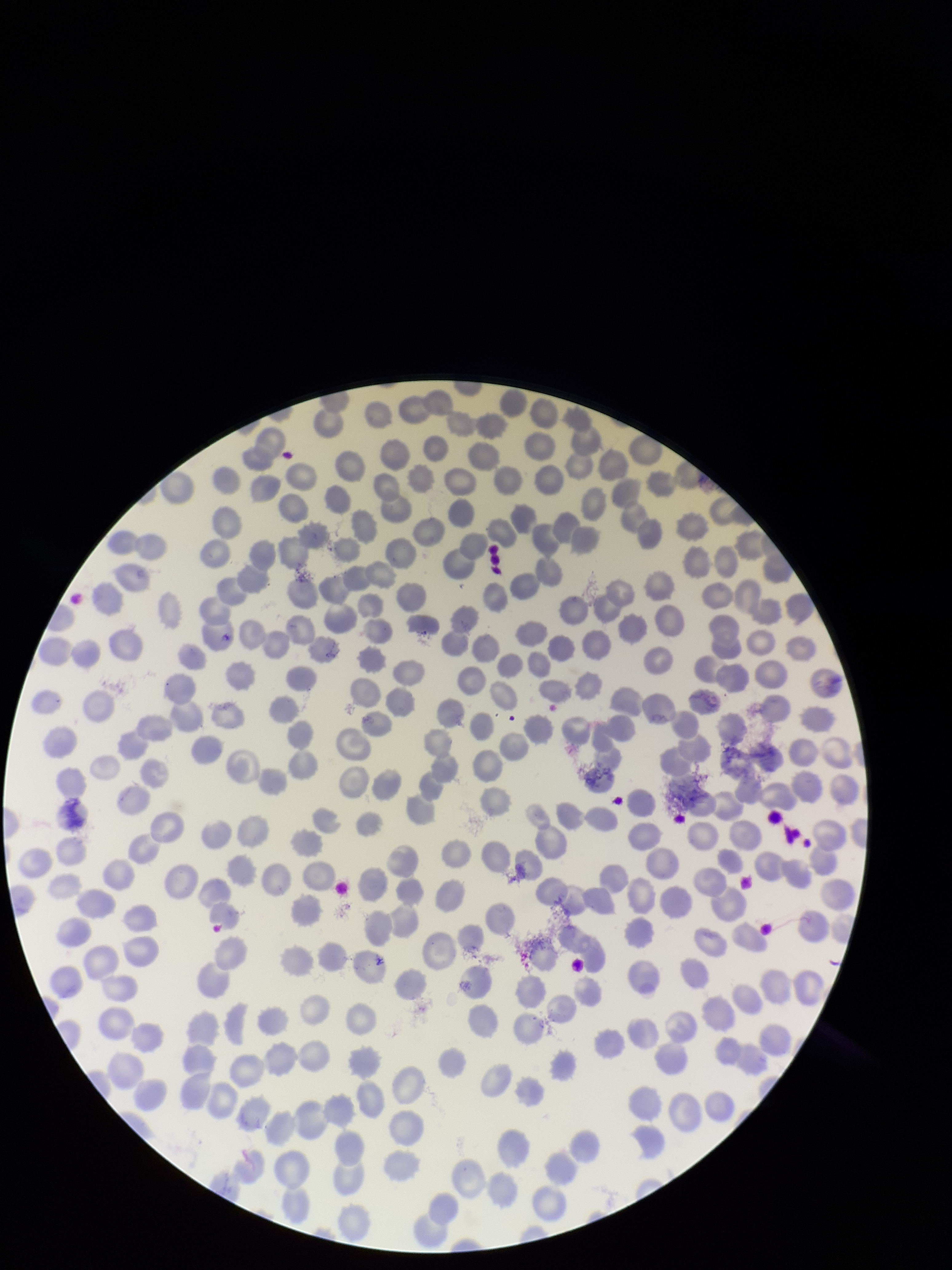

parasitized red blood cells = none seen
parasitized red blood cell count = 0
stain = Giemsa
red blood cell count = 282
patient malaria status = positive
image size = 952×1270 pixels
preparation = thin
field of view = one from this slide
species reported for this patient = Plasmodium falciparum
capture = smartphone photograph through the microscope eyepiece